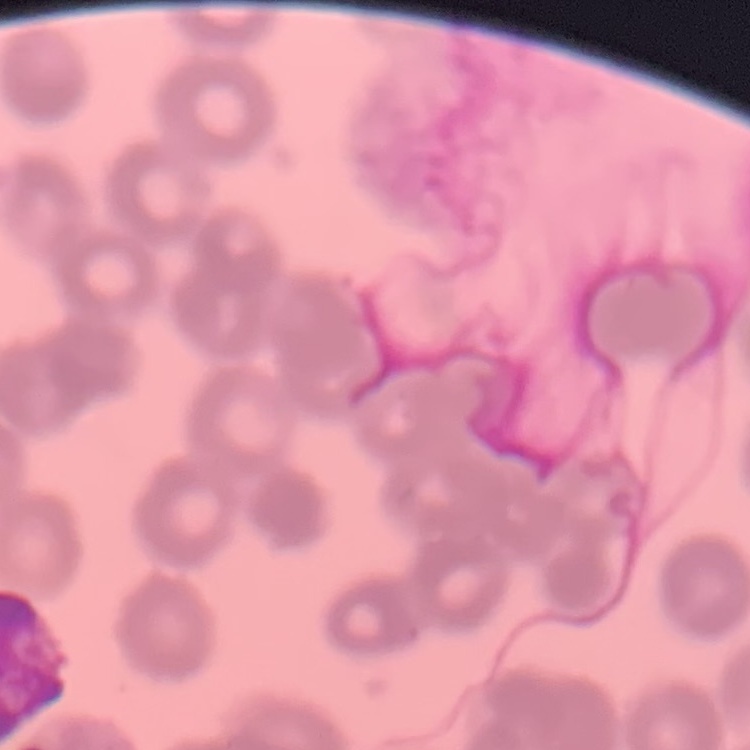
The red blood cells exhibit rouleaux formation. One tile cut from a larger photomicrograph. Stained with either Field's or Giemsa. Thin blood smear.